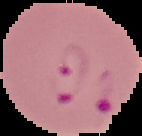
image size = 142×136 pixels
malaria status = parasitized
preparation = thin blood smear
image type = cell region segmented out of the field of view; surrounding area masked to black